State the blood parasite species.
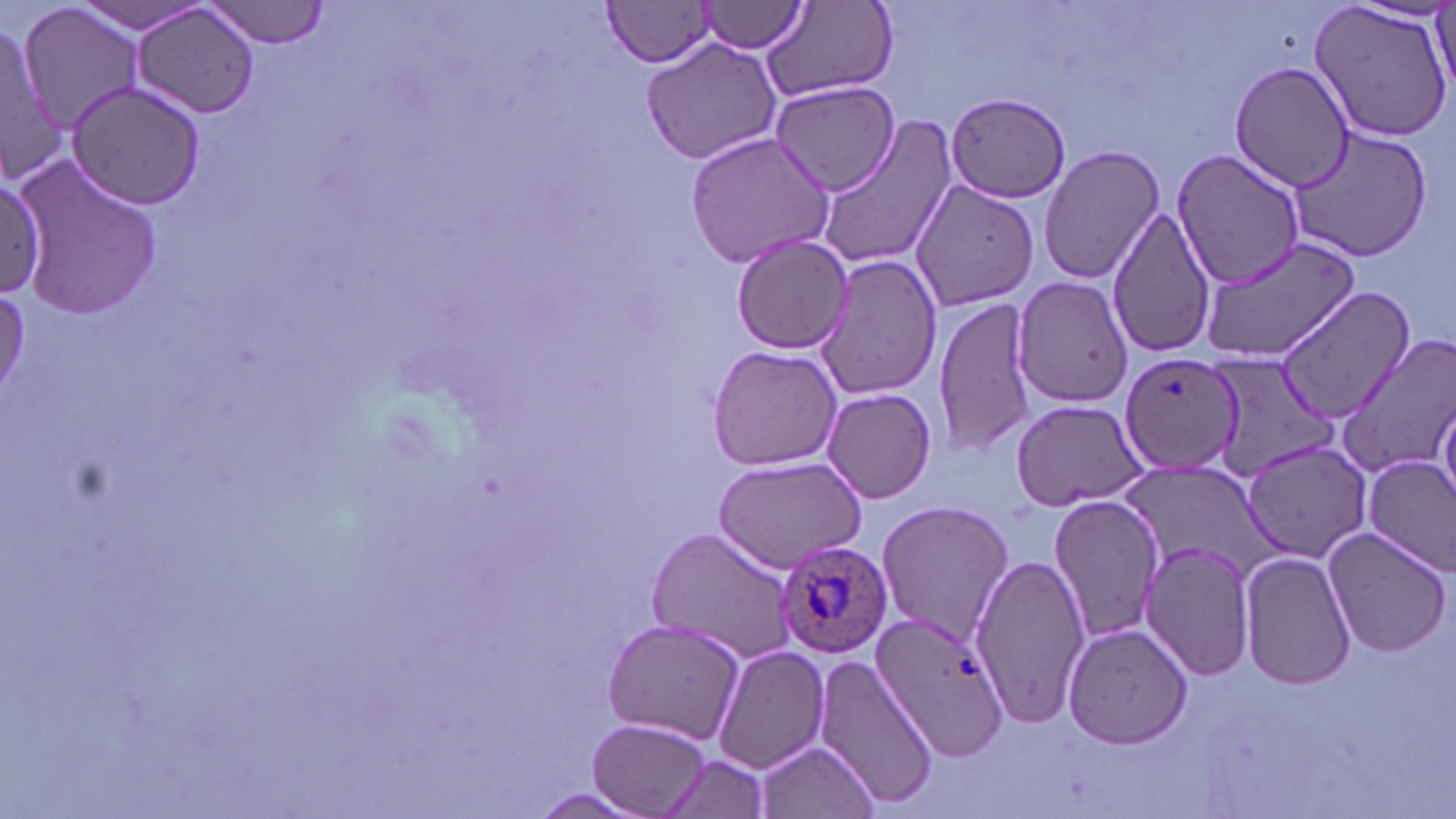

Plasmodium ovale.

preparation = thin blood smear
field of view = one of a larger specimen
Plasmodium ovale-infected red blood cell locations = approximate bounding boxes as named x1/y1/x2/y2 corners in pixels: (x1=774, y1=540, x2=894, y2=660)
modality = light microscopy
uninfected red blood cell locations = approximate bounding boxes as named x1/y1/x2/y2 corners in pixels: (x1=202, y1=0, x2=332, y2=48), (x1=700, y1=0, x2=806, y2=53), (x1=761, y1=0, x2=898, y2=105), (x1=1430, y1=0, x2=1454, y2=97), (x1=66, y1=1, x2=215, y2=35), (x1=131, y1=2, x2=262, y2=119), (x1=1309, y1=2, x2=1454, y2=145), (x1=604, y1=3, x2=715, y2=67), (x1=16, y1=4, x2=145, y2=135), (x1=0, y1=21, x2=62, y2=181), (x1=642, y1=37, x2=784, y2=164), (x1=1229, y1=60, x2=1357, y2=193), (x1=64, y1=80, x2=207, y2=210), (x1=772, y1=80, x2=902, y2=196), (x1=943, y1=91, x2=1072, y2=203), (x1=815, y1=116, x2=957, y2=272), (x1=1287, y1=128, x2=1435, y2=263), (x1=684, y1=129, x2=838, y2=271), (x1=1038, y1=145, x2=1166, y2=284), (x1=1173, y1=151, x2=1307, y2=290), (x1=10, y1=153, x2=161, y2=322), (x1=0, y1=177, x2=50, y2=301), (x1=907, y1=178, x2=1038, y2=313), (x1=1106, y1=205, x2=1218, y2=359), (x1=730, y1=233, x2=853, y2=353), (x1=1199, y1=236, x2=1362, y2=362), (x1=812, y1=255, x2=944, y2=402), (x1=1013, y1=276, x2=1133, y2=408), (x1=1273, y1=286, x2=1415, y2=426), (x1=933, y1=294, x2=1038, y2=454), (x1=1335, y1=335, x2=1456, y2=478), (x1=706, y1=343, x2=844, y2=471), (x1=1120, y1=354, x2=1244, y2=476), (x1=1204, y1=354, x2=1336, y2=482), (x1=821, y1=388, x2=939, y2=504), (x1=1435, y1=395, x2=1455, y2=508), (x1=1009, y1=399, x2=1147, y2=510), (x1=1239, y1=439, x2=1373, y2=564), (x1=1365, y1=455, x2=1456, y2=576), (x1=710, y1=456, x2=866, y2=570), (x1=1048, y1=494, x2=1165, y2=647), (x1=876, y1=498, x2=1014, y2=645), (x1=645, y1=526, x2=798, y2=663), (x1=1320, y1=526, x2=1452, y2=657), (x1=1139, y1=538, x2=1255, y2=683), (x1=1238, y1=550, x2=1356, y2=691), (x1=969, y1=554, x2=1092, y2=724), (x1=856, y1=609, x2=1010, y2=771), (x1=601, y1=618, x2=747, y2=745), (x1=1062, y1=624, x2=1193, y2=750), (x1=712, y1=644, x2=831, y2=776), (x1=813, y1=653, x2=938, y2=806), (x1=589, y1=719, x2=711, y2=816), (x1=755, y1=739, x2=881, y2=818), (x1=660, y1=757, x2=773, y2=818)
magnification = 1000x
image size = 1456×819 pixels
stain = May-Grünwald-Giemsa